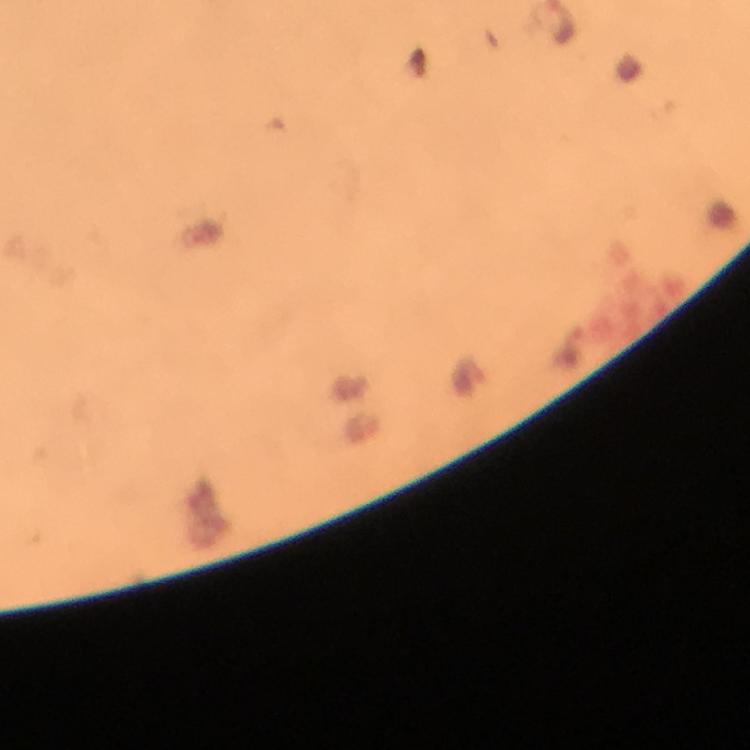
Approximate centers as (x, y) in pixels.
Summary:
  - Malaria parasite locations: (470, 376)
  - Capture: smartphone camera through the microscope
  - Immersion oil: applied
  - Magnification: 100x
  - Preparation: thick blood smear
  - Context: from a diagnostic examination for malaria
  - Stain: Giemsa
  - Image size: 750×750 pixels
  - Cropped from: a single field of view